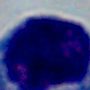
modality: micrograph
identification: white blood cell
magnification: 1000x